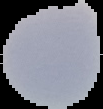

Summary:
  - Malaria status: uninfected
  - Image type: segmented cell region with the area outside set to black
  - Image size: 103×109 pixels
  - Preparation: thin blood film